Classify this cell by malaria status.
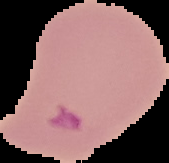
It is parasitized.

From a thin blood smear. Image is 169×163 pixels. Segmented cell region on a black background.